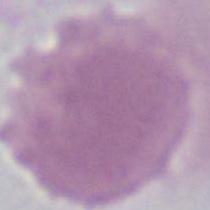

Summary:
  - Modality: micrograph
  - Magnification: 1000x
  - Identification: erythrocyte